Assess this cell for malaria.
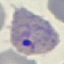

It is parasitized.

Thin blood smear. Giemsa stain. Cell patch, automatically extracted from a larger field of view and resized to 64 × 64 pixels. Acquired by smartphone through the microscope eyepiece.